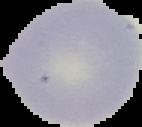 From a thin blood film. Image is 142×127 pixels. Malaria status: uninfected. Cell region segmented out of the field of view; the surrounding area is masked to black.